Assess this cell for malaria.
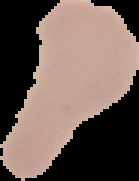

Uninfected.

{
  "image_type": "segmented cell region on a black background",
  "image_size": "139×181 pixels",
  "preparation": "thin blood smear"
}